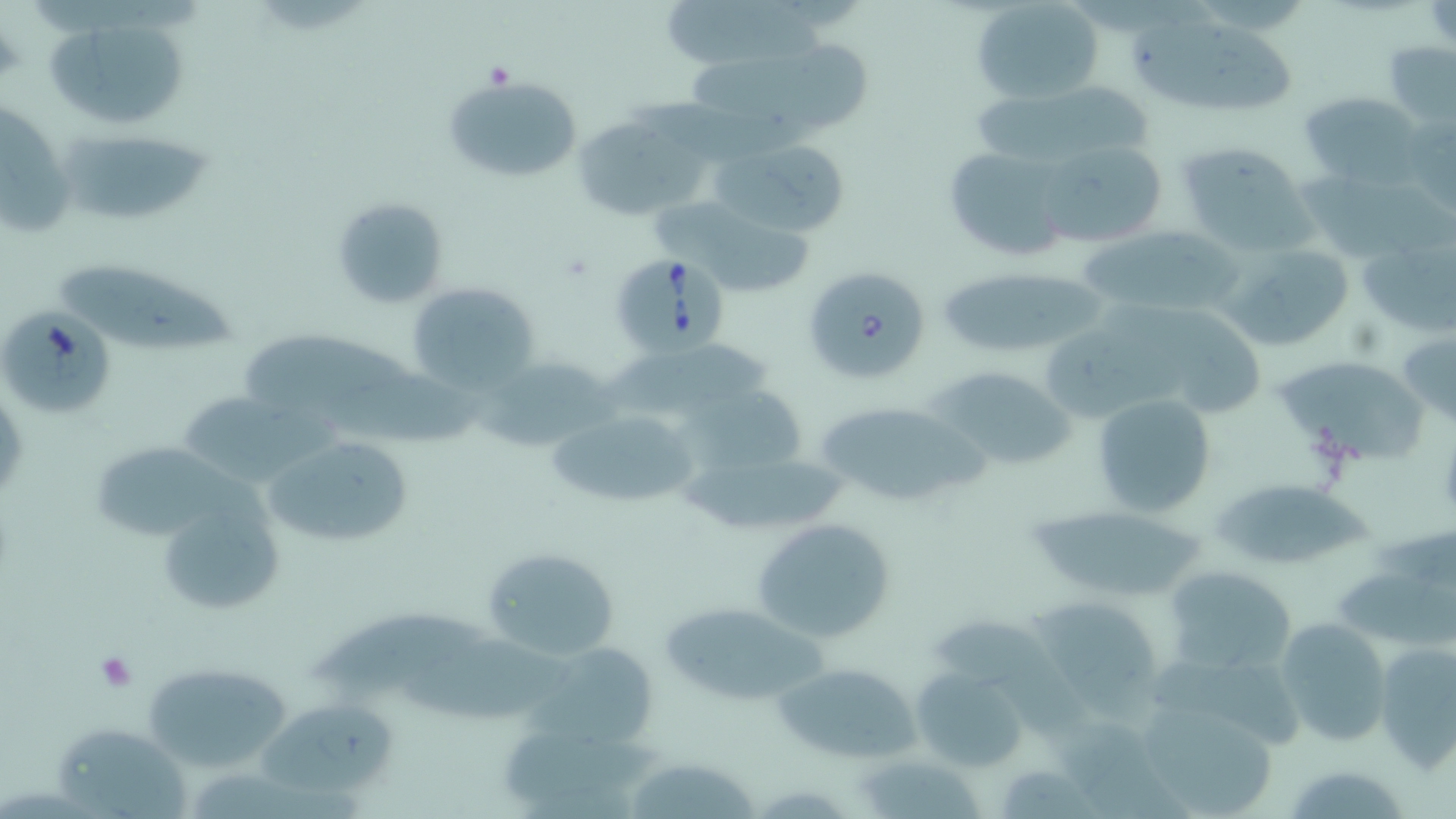

Approximate bounding boxes as (x1, y1, x2, y2) in pixels. Babesia divergens-infected red blood cell locations: (620, 254, 727, 362), (803, 266, 931, 386). Platelet locations: (92, 649, 140, 692). Uninfected red blood cell locations: (972, 0, 1103, 104), (659, 4, 831, 68), (1129, 16, 1297, 110), (45, 28, 188, 125), (684, 42, 875, 132), (1383, 42, 1455, 129), (442, 72, 584, 184), (972, 87, 1152, 156), (1300, 90, 1421, 184), (1, 99, 75, 239), (576, 118, 716, 215), (50, 134, 213, 225), (718, 140, 852, 238), (1034, 140, 1174, 250), (1175, 142, 1317, 254), (936, 143, 1081, 264), (1300, 168, 1456, 263), (329, 196, 449, 309), (649, 197, 814, 293), (1076, 222, 1244, 321), (1359, 236, 1452, 336), (1221, 243, 1355, 351), (52, 259, 241, 357), (931, 266, 1116, 359), (407, 281, 537, 392), (1165, 294, 1268, 425), (1040, 302, 1174, 430), (3, 309, 119, 418), (1399, 330, 1456, 428), (245, 332, 488, 450), (477, 355, 615, 455), (1278, 355, 1422, 468), (928, 365, 1078, 474), (179, 390, 348, 486), (1091, 393, 1215, 518), (815, 400, 979, 510), (542, 406, 704, 511), (262, 433, 417, 553), (93, 441, 279, 543), (676, 442, 850, 537), (1211, 478, 1373, 573), (1025, 504, 1207, 600), (752, 518, 896, 642), (480, 543, 625, 661), (1163, 565, 1296, 678), (1337, 567, 1456, 651), (1023, 595, 1173, 714), (307, 601, 485, 697), (661, 601, 824, 706), (936, 611, 1097, 741), (1275, 617, 1391, 748), (406, 631, 571, 718), (522, 642, 665, 752), (1374, 642, 1456, 774), (771, 658, 924, 764), (148, 662, 288, 770), (909, 666, 1031, 774), (1135, 694, 1287, 817), (259, 699, 391, 788), (1055, 709, 1200, 819), (54, 723, 194, 819), (619, 754, 764, 819), (192, 758, 371, 819), (1281, 764, 1414, 819). Slide-level diagnosis: Babesia divergens. May-Grünwald-Giemsa stain. Optical microscopy. Captured at 1000x magnification. Image is 1456×819 pixels. Single field of view. Thin blood smear.